Evaluate for Plasmodium parasites.
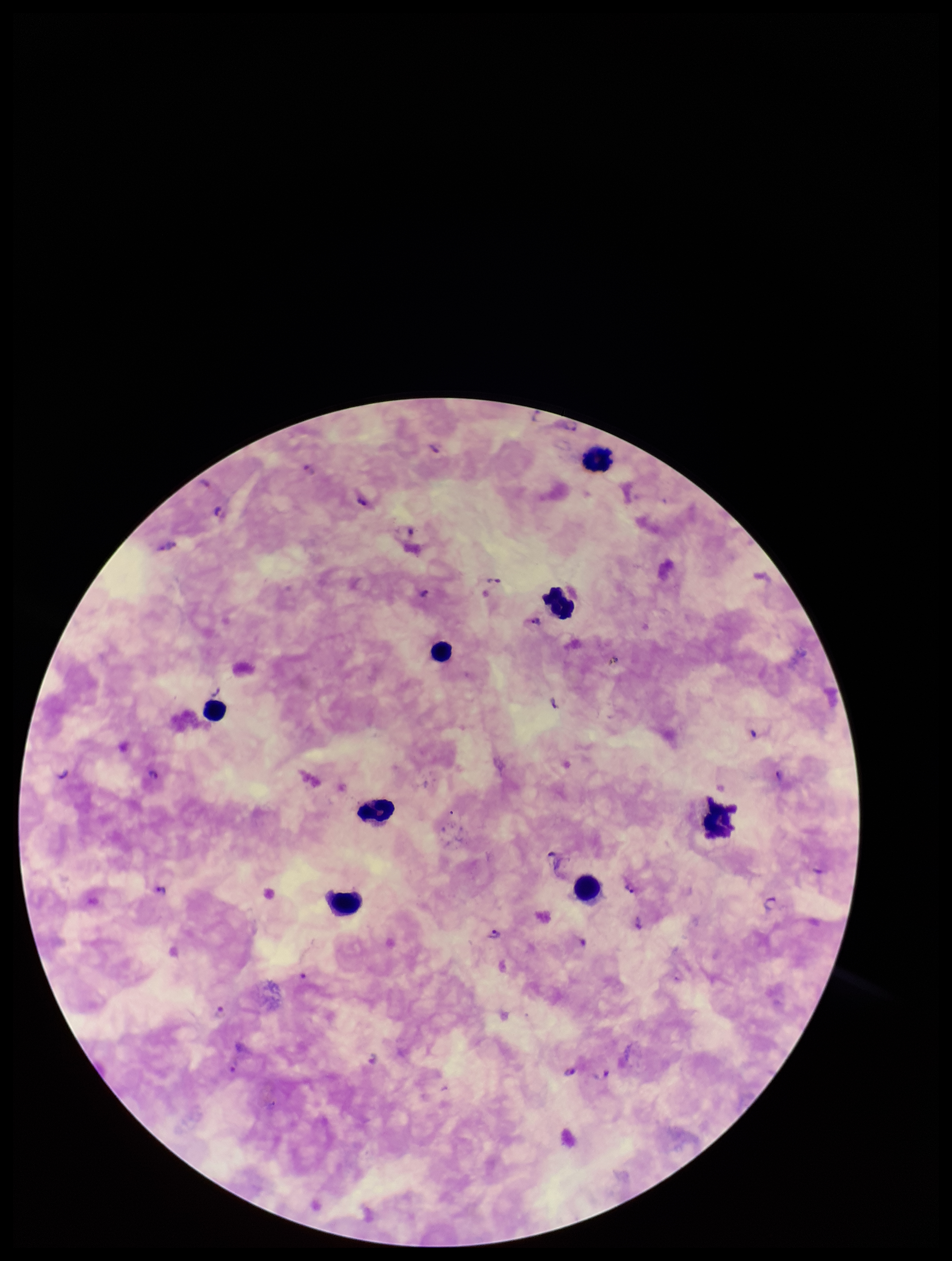
Seen.

parasite_count: 28
image_size: 952×1261 pixels
species_reported_for_this_patient: Plasmodium falciparum
field_of_view: one from this slide
preparation: thick
capture: smartphone photograph through the microscope eyepiece
stain: Giemsa
leukocyte_count: 8
patient_malaria_status: infected